Classify this cell by malaria status.
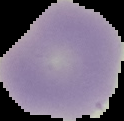
It is uninfected.

From a thin blood film. Segmented cell region on a black background. Image is 124×121 pixels.